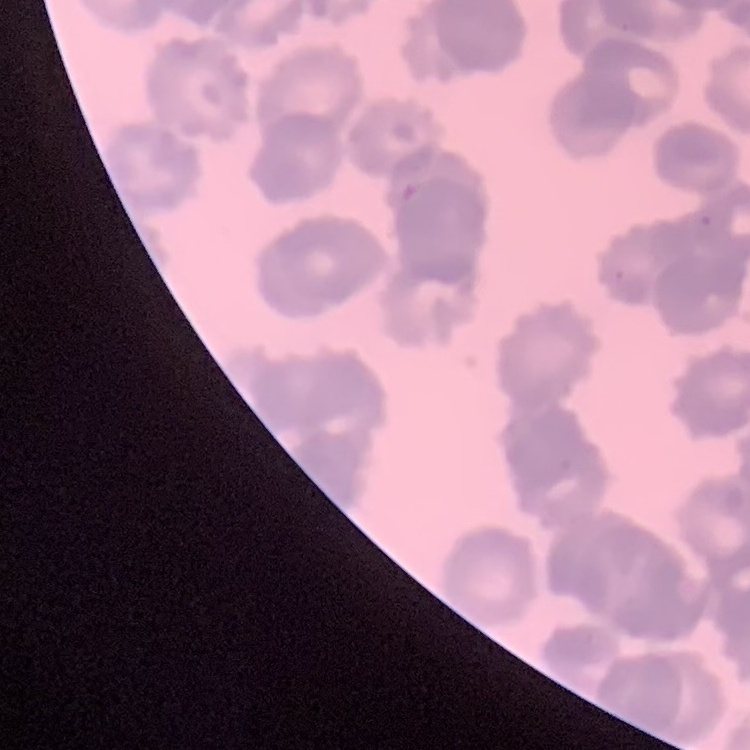
The erythrocytes exhibit rouleaux formation. Square crop of a larger photomicrograph. Thin blood smear. Field's or Giemsa stain.